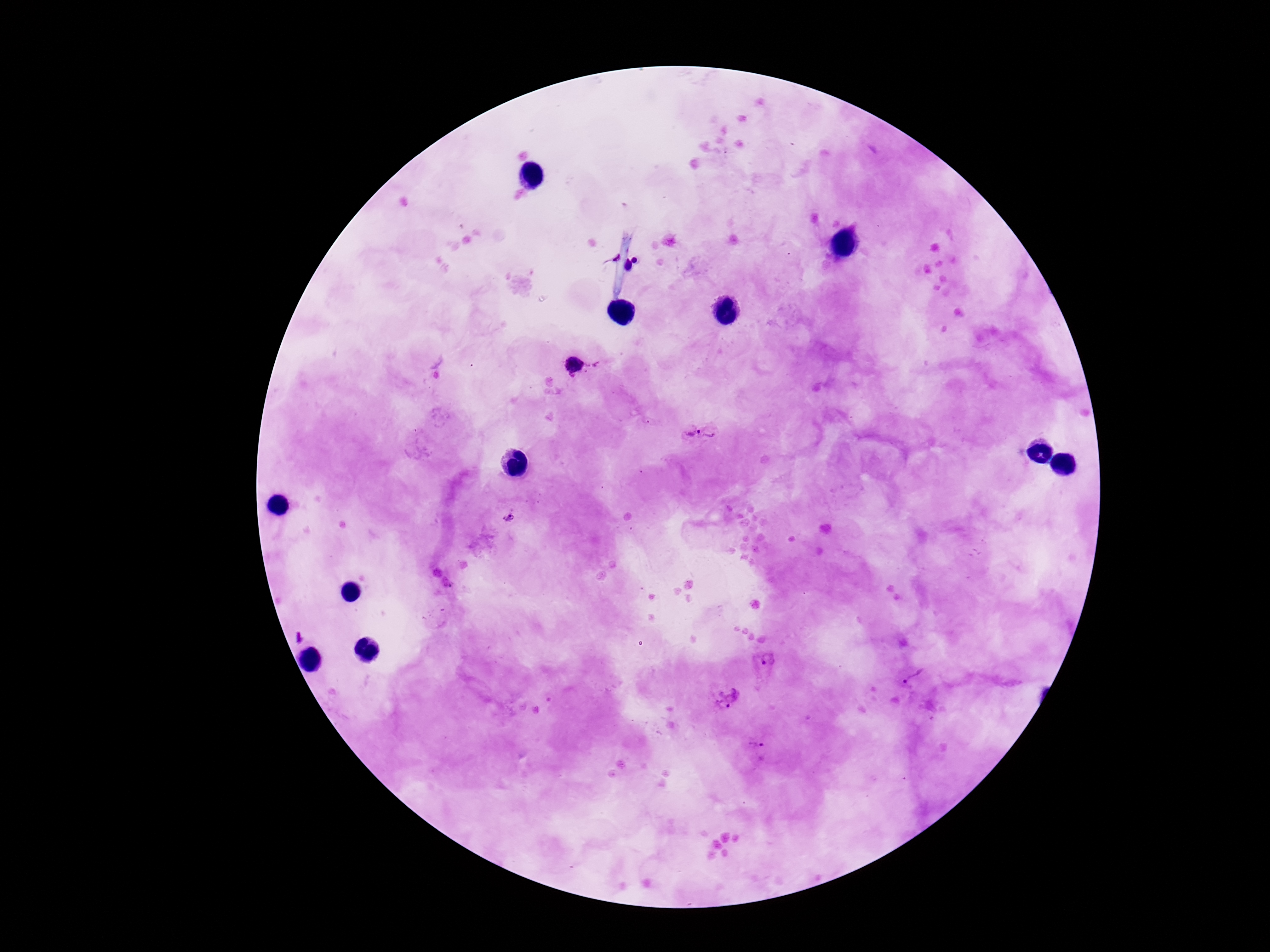

{
  "preparation": "thick blood film",
  "plasmodium_parasite_locations": "approximate object centers, in pixels from the top-left corner: (x=602, y=365), (x=574, y=366), (x=700, y=433), (x=510, y=517), (x=769, y=660), (x=913, y=678), (x=724, y=696), (x=758, y=751)",
  "magnification": "100x",
  "capture": "smartphone camera through the microscope eyepiece",
  "patient_malaria_status": "positive",
  "field_of_view": "single",
  "image_size": "1270×952 pixels",
  "stain": "Giemsa"
}